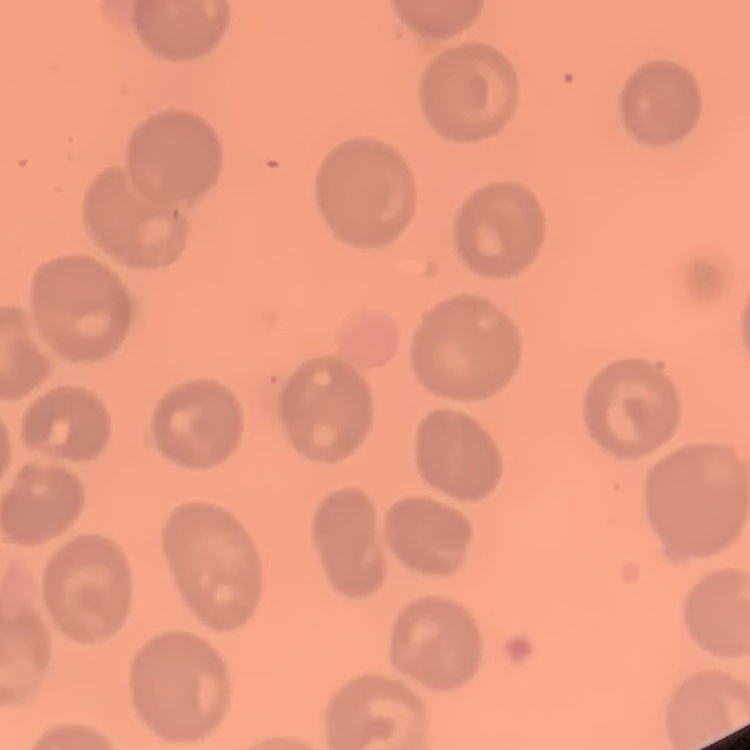

Summary:
  - Erythrocyte morphology: no rouleaux formation
  - Preparation: thin blood smear
  - Image type: square crop of a larger photomicrograph
  - Stain: Field's or Giemsa